Assess this cell for malaria.
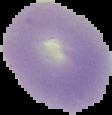
It is uninfected.

Image is 112×115 pixels. From a thin blood film. Segmented cell region on a black background.